Describe the morphology of the erythrocytes.
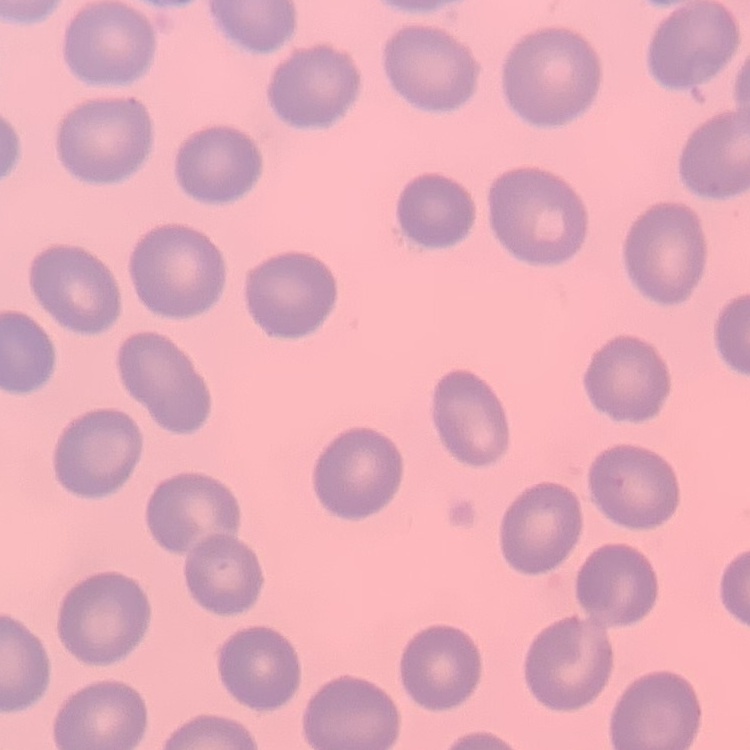
No rouleaux formation.

image type = one tile cut from a larger photomicrograph
stain = Field's or Giemsa
preparation = thin peripheral smear